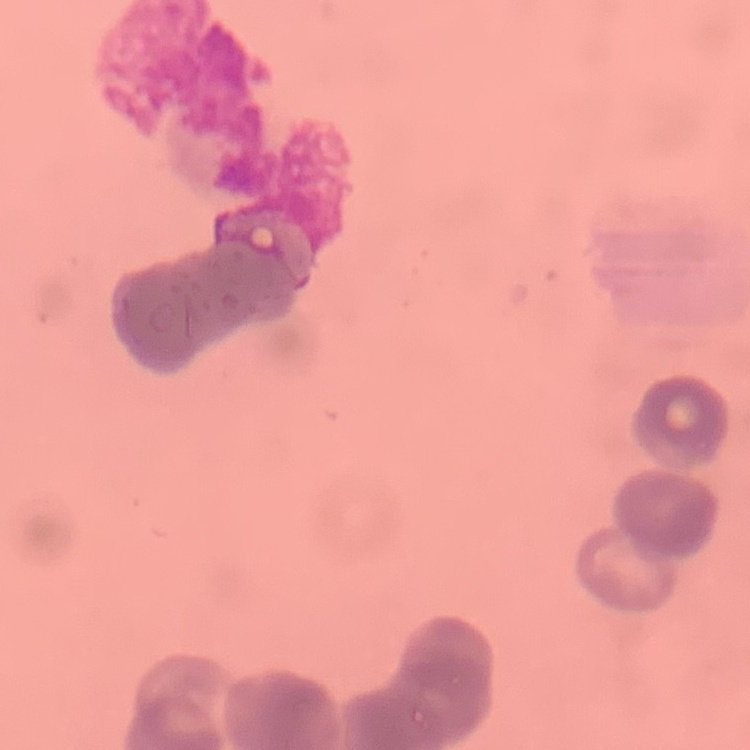 The red blood cells exhibit rouleaux formation. Field's or Giemsa stain. Square crop of a larger photomicrograph. Thin peripheral smear.